Identify the parasite.
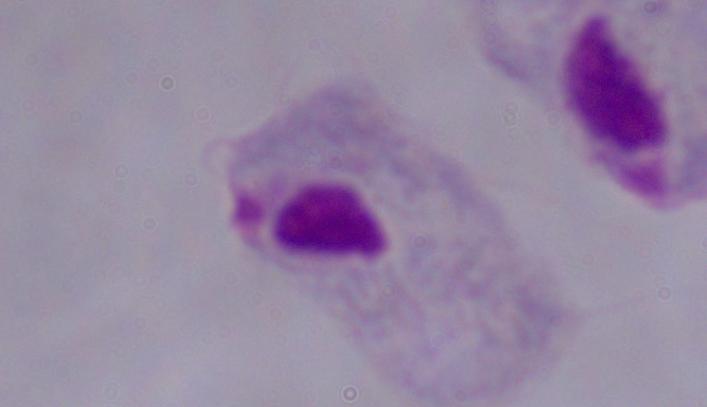
This is a trichomonad.

Summary:
  - Modality: photomicrograph
  - Magnification: 1000x